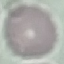

Summary:
  - Malaria status: uninfected
  - Capture: smartphone camera at the microscope eyepiece
  - Preparation: thin blood smear
  - Stain: Giemsa
  - Image type: automatically extracted cell patch, resized to 64 × 64 pixels